Classify this cell by malaria status.
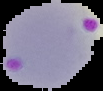

It is parasitized.

Summary:
  - Preparation: thin blood smear
  - Image type: segmented cell region with the area outside set to black
  - Image size: 103×91 pixels